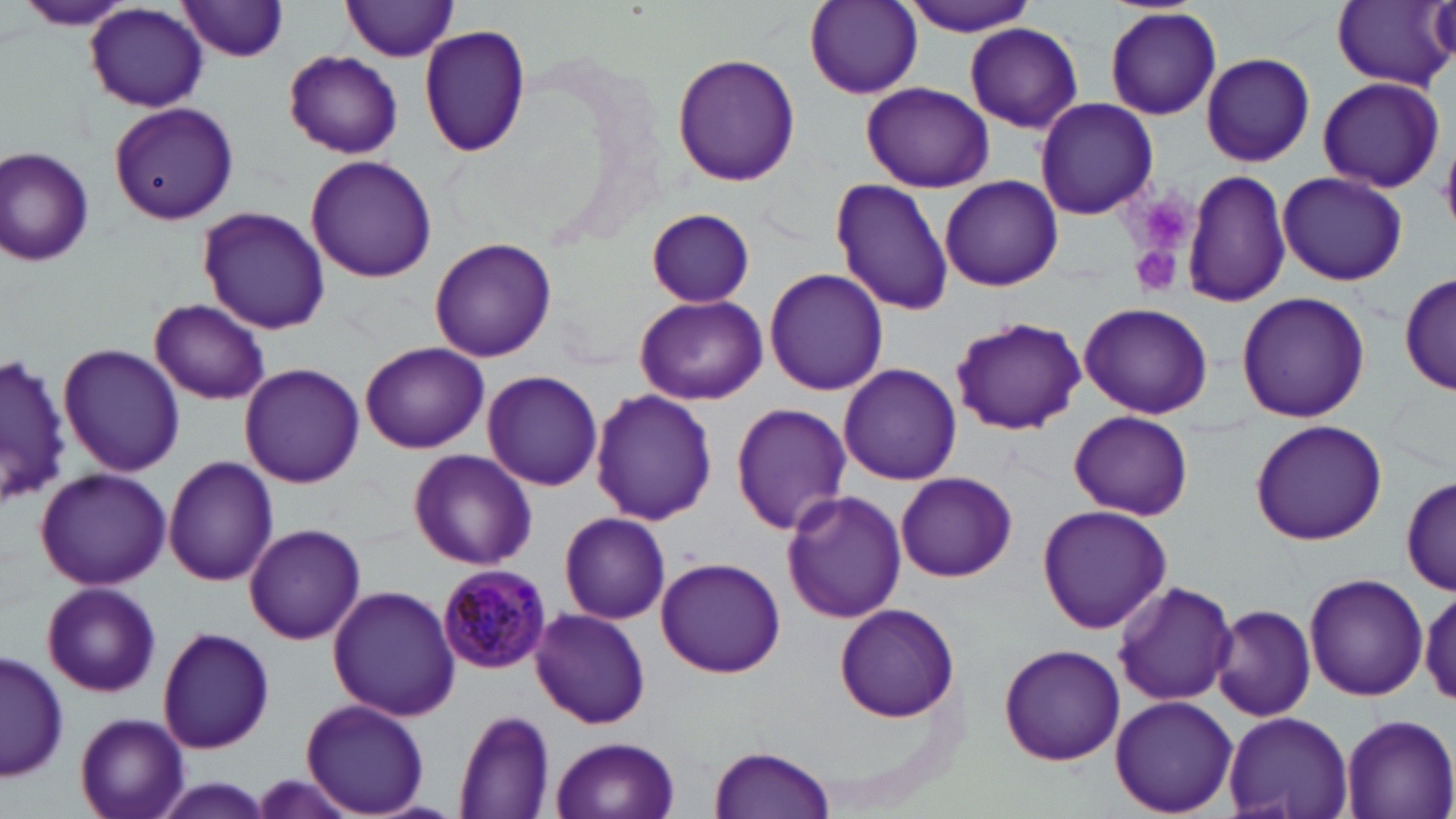

Summary:
  - Coordinate format: approximate bounding boxes as (x1,y1)-(x2,y2) corner pairs in pixels
  - Plasmodium malariae-infected red blood cell locations: (435,563)-(554,672)
  - Platelet locations: (1141,195)-(1189,241), (1130,245)-(1183,297)
  - Uninfected red blood cell locations: (896,0)-(1040,36), (16,1)-(137,32), (177,1)-(291,60), (341,1)-(462,62), (806,1)-(923,99), (1332,2)-(1452,90), (84,3)-(209,113), (1102,6)-(1223,122), (418,22)-(529,158), (964,24)-(1083,133), (283,50)-(403,159), (1200,52)-(1316,168), (670,53)-(801,186), (1316,76)-(1446,193), (862,82)-(993,193), (1033,98)-(1158,219), (108,102)-(237,225), (0,145)-(97,269), (305,156)-(438,283), (1183,167)-(1290,308), (1277,170)-(1408,286), (939,175)-(1063,292), (829,177)-(955,316), (196,207)-(331,334), (646,207)-(755,307), (429,239)-(555,363), (764,267)-(887,396), (1401,270)-(1456,399), (1235,290)-(1371,423), (634,295)-(769,404), (151,298)-(270,403), (1079,301)-(1213,419), (949,315)-(1087,434), (360,342)-(488,454), (57,343)-(185,475), (1,352)-(69,509), (839,362)-(963,485), (240,363)-(366,487), (482,370)-(603,492), (589,387)-(717,525), (731,402)-(851,536), (1068,410)-(1193,521), (1249,419)-(1387,545), (408,450)-(537,570), (163,457)-(279,588), (34,466)-(173,590), (895,472)-(1018,581), (1399,472)-(1453,598), (780,490)-(908,624), (1036,503)-(1171,633), (558,511)-(671,625), (243,523)-(365,645), (655,556)-(786,678), (1303,572)-(1429,702), (1110,577)-(1240,708), (40,580)-(160,698), (1416,583)-(1456,707), (327,586)-(460,722), (833,604)-(961,721), (1209,604)-(1316,722), (528,607)-(652,730), (157,627)-(275,756), (997,642)-(1126,767), (1,651)-(66,782), (1109,696)-(1238,817), (300,698)-(430,816), (454,710)-(556,818), (1224,710)-(1354,819), (75,711)-(190,819), (1338,712)-(1455,819), (552,735)-(680,819), (710,744)-(835,819), (152,779)-(272,817)
  - Slide-level diagnosis: Plasmodium malariae
  - Magnification: 1000x
  - Field of view: single
  - Stain: May-Grünwald-Giemsa
  - Modality: optical microscopy
  - Preparation: thin blood smear
  - Image size: 1456×819 pixels